State which parasite is depicted.
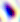
This is Toxoplasma gondii.

magnification = 400x
modality = micrograph